Report the malaria status of this cell.
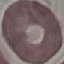
Uninfected.

capture: smartphone camera at the microscope eyepiece
stain: Giemsa
image_type: automatically extracted cell patch, resized to 64 × 64 pixels
preparation: thin blood film